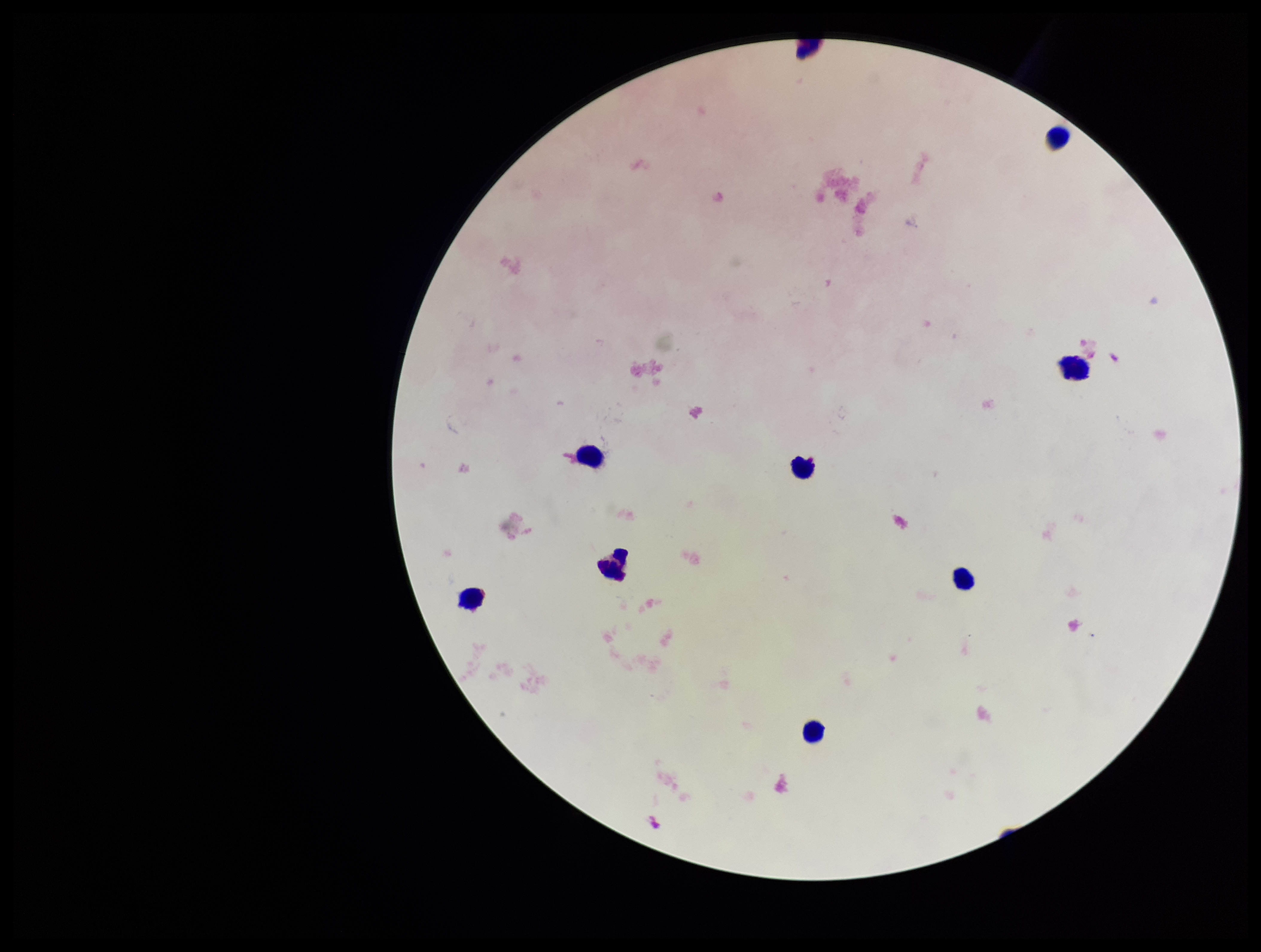
Stained with Giemsa. Single field of view. Preparation: thick. Smartphone photograph taken through the eyepiece of a microscope. Image is 1261×952 pixels. Parasite count: 0. Patient malaria status: negative. Leukocyte count: 8. Plasmodium parasites: none detected.